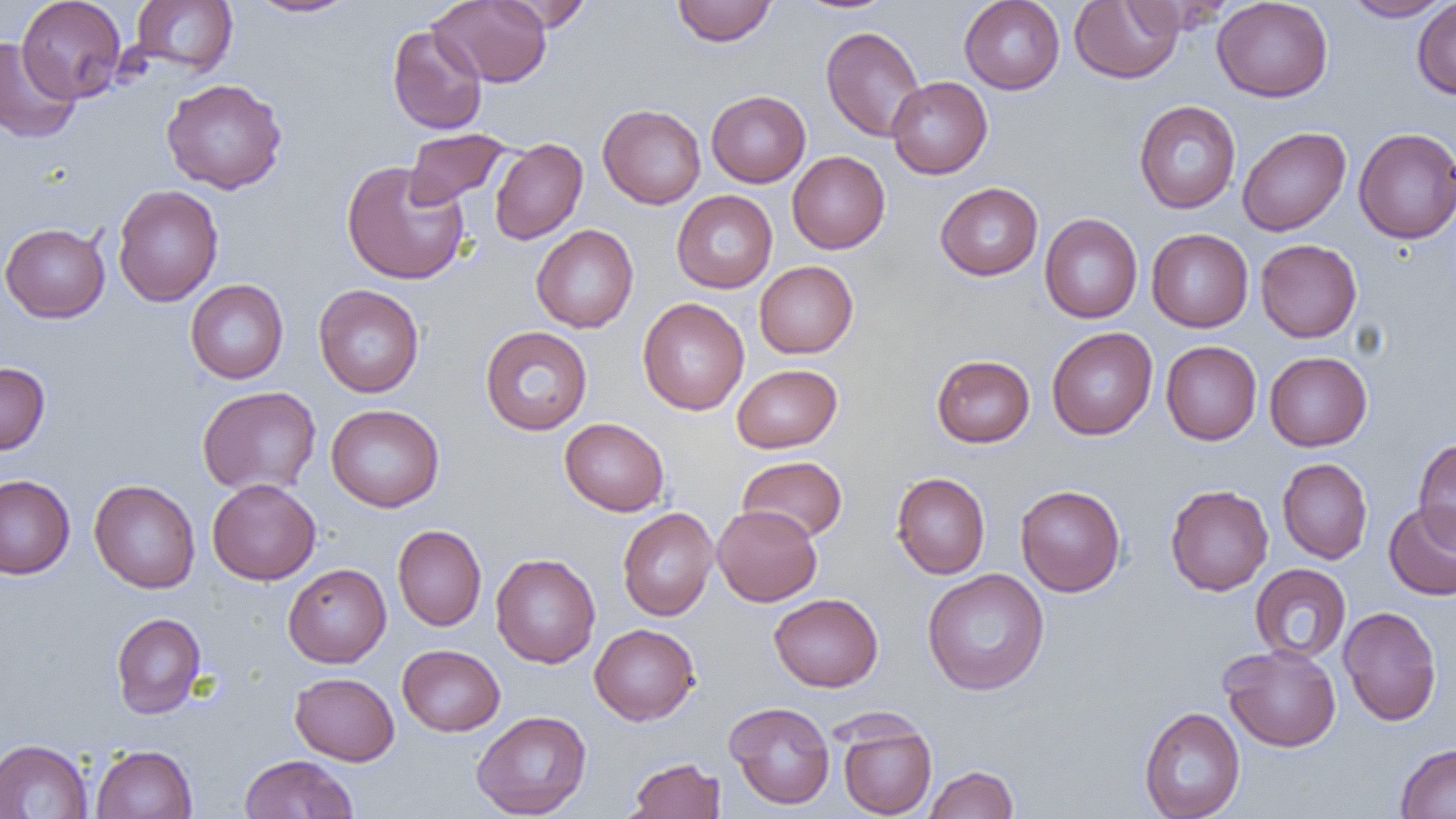
Summary:
  - Coordinate format: approximate bounding boxes as (x1, y1, x2, y2) in pixels
  - Uninfected red blood cell locations: (17, 0, 127, 103), (130, 0, 238, 76), (247, 0, 358, 18), (430, 0, 552, 87), (792, 0, 900, 15), (959, 0, 1065, 94), (1069, 0, 1183, 84), (1212, 0, 1333, 102), (1341, 0, 1451, 21), (1412, 0, 1456, 100), (492, 1, 594, 32), (672, 1, 777, 46), (386, 25, 487, 135), (821, 26, 926, 142), (0, 37, 81, 144), (886, 76, 992, 179), (161, 78, 288, 194), (706, 90, 810, 187), (1133, 100, 1241, 214), (598, 104, 706, 209), (1237, 127, 1350, 236), (1353, 128, 1456, 244), (404, 129, 511, 209), (489, 138, 587, 245), (787, 151, 890, 253), (341, 160, 470, 285), (935, 182, 1043, 281), (112, 184, 224, 307), (671, 190, 777, 293), (1040, 214, 1143, 323), (0, 222, 110, 323), (531, 225, 638, 332), (1146, 228, 1253, 332), (1255, 239, 1362, 342), (754, 261, 858, 358), (185, 279, 289, 384), (313, 284, 424, 398), (637, 298, 749, 415), (480, 326, 593, 435), (1046, 327, 1158, 440), (1161, 341, 1262, 445), (1264, 351, 1372, 451), (931, 354, 1035, 447), (0, 362, 50, 455), (731, 364, 842, 453), (197, 385, 322, 496), (326, 404, 445, 512), (559, 418, 669, 516), (1413, 439, 1456, 550), (737, 455, 847, 542), (1277, 458, 1373, 564), (891, 472, 990, 579), (0, 474, 75, 579), (207, 478, 321, 585), (89, 479, 201, 593), (1015, 484, 1126, 596), (1165, 484, 1273, 596), (1383, 501, 1456, 601), (712, 504, 822, 606), (618, 507, 718, 620), (392, 524, 486, 631), (491, 553, 601, 668), (283, 563, 391, 667), (1250, 563, 1351, 663), (922, 568, 1050, 695), (770, 593, 883, 692), (1338, 606, 1442, 726), (111, 612, 207, 718), (589, 623, 700, 725), (397, 644, 505, 736), (1219, 644, 1341, 752), (290, 672, 400, 765), (724, 701, 835, 809), (1139, 706, 1245, 819), (472, 710, 592, 818), (836, 715, 937, 819), (0, 738, 93, 819), (1395, 743, 1456, 819), (91, 744, 197, 819), (239, 754, 359, 818), (626, 756, 725, 819), (923, 765, 1019, 819)
  - Slide-level diagnosis: no evidence of blood parasites
  - Field of view: single
  - Image size: 1456×819 pixels
  - Modality: optical microscopy
  - Preparation: thin blood smear
  - Magnification: 1000x